Outline platelets.
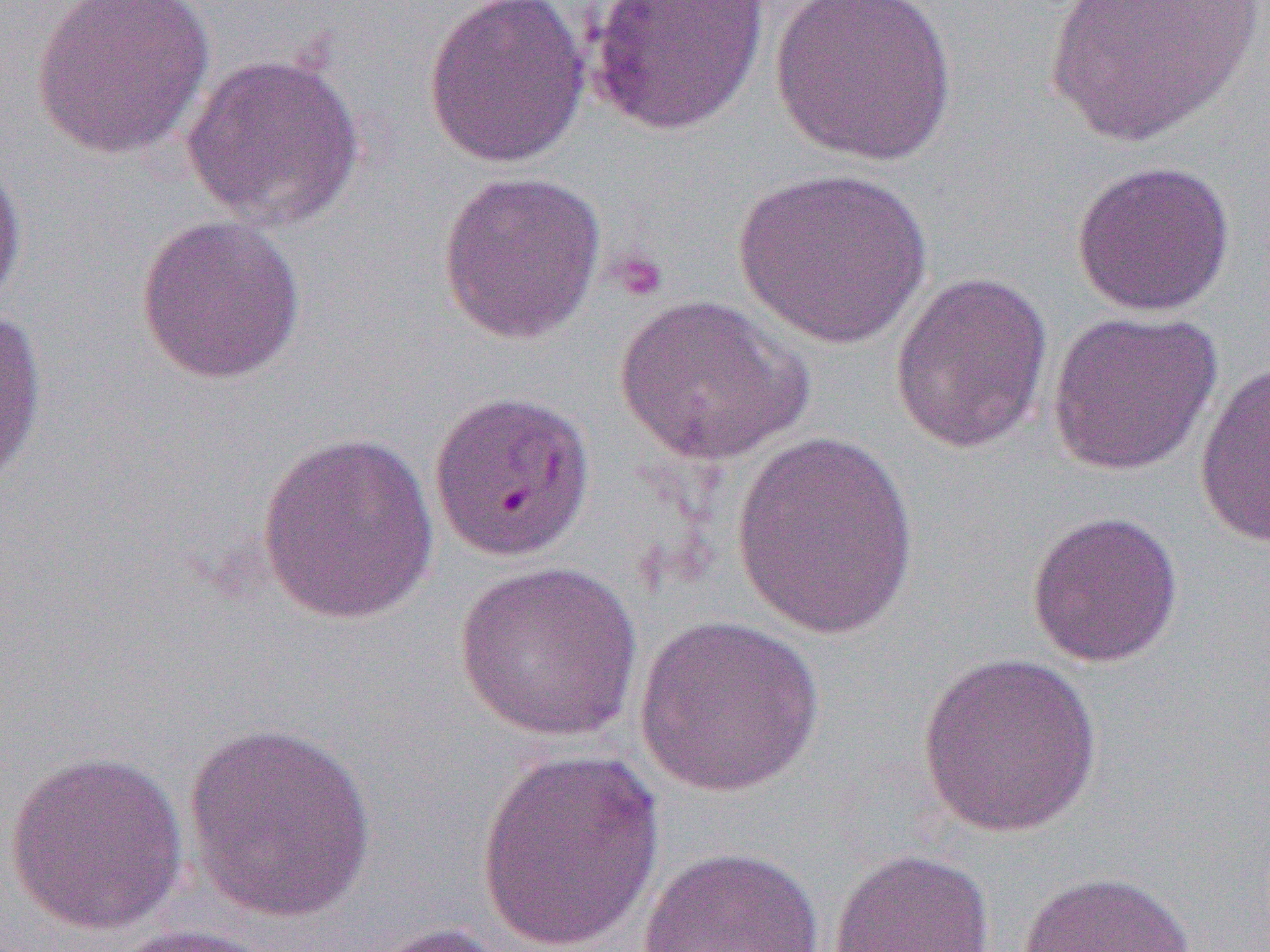

Approximate bounding boxes as (x1, y1, x2, y2) in pixels.
Platelets: (609, 249, 668, 302).

slide-level diagnosis = Plasmodium falciparum
image size = 1270×952 pixels
field of view = single
preparation = thin blood smear
uninfected red blood cell locations = approximate bounding boxes as (x1, y1, x2, y2) in pixels: (29, 0, 217, 158), (421, 0, 591, 169), (586, 0, 770, 137), (768, 0, 959, 168), (1039, 0, 1262, 150), (180, 50, 366, 231), (0, 151, 29, 316), (1070, 159, 1236, 318), (733, 167, 933, 350), (437, 170, 607, 346), (135, 214, 307, 385), (888, 270, 1054, 455), (614, 294, 811, 466), (0, 303, 49, 492), (1046, 309, 1221, 477), (1194, 362, 1270, 551), (729, 429, 920, 640), (255, 431, 440, 626), (1026, 511, 1184, 668), (453, 560, 642, 741), (633, 614, 826, 798), (915, 650, 1103, 837), (182, 720, 378, 923), (4, 747, 191, 936), (475, 748, 666, 952), (637, 845, 826, 952), (829, 847, 996, 952), (1016, 869, 1197, 952), (354, 920, 521, 952), (105, 923, 290, 952)
magnification = 1000x
modality = light microscopy